Identify the cell.
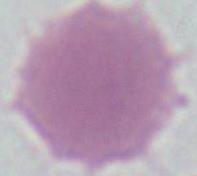

An erythrocyte.

Photomicrograph. 1000x magnification.